Comment on the morphology of the red blood cells.
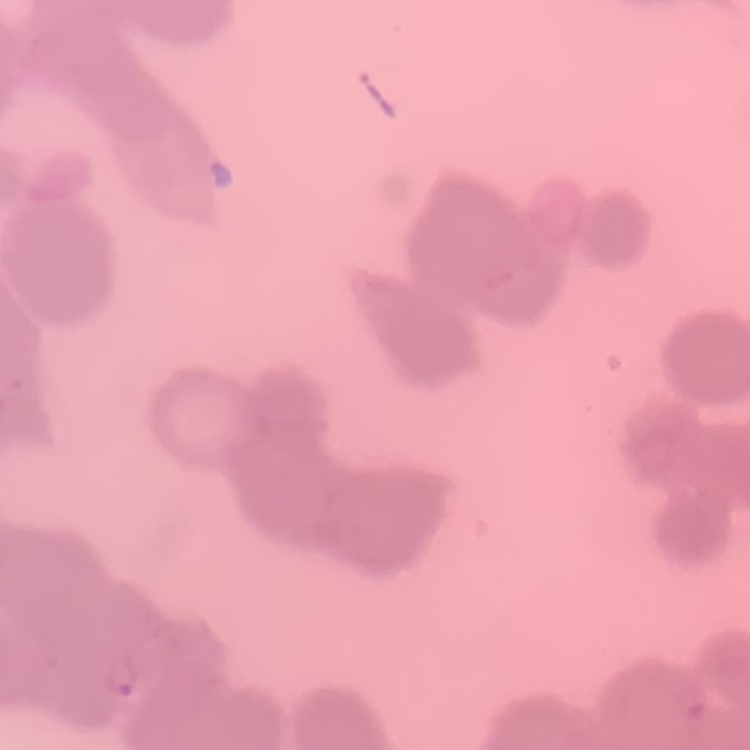
Rouleaux formation.

{
  "image_type": "square crop of a larger photomicrograph",
  "preparation": "thin blood smear",
  "stain": "Field's or Giemsa"
}